Classify this cell by malaria status.
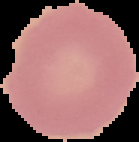

Uninfected.

image type = cell region segmented out of the field of view; surrounding area masked to black
image size = 139×142 pixels
preparation = thin blood smear